Comment on the morphology of the erythrocytes.
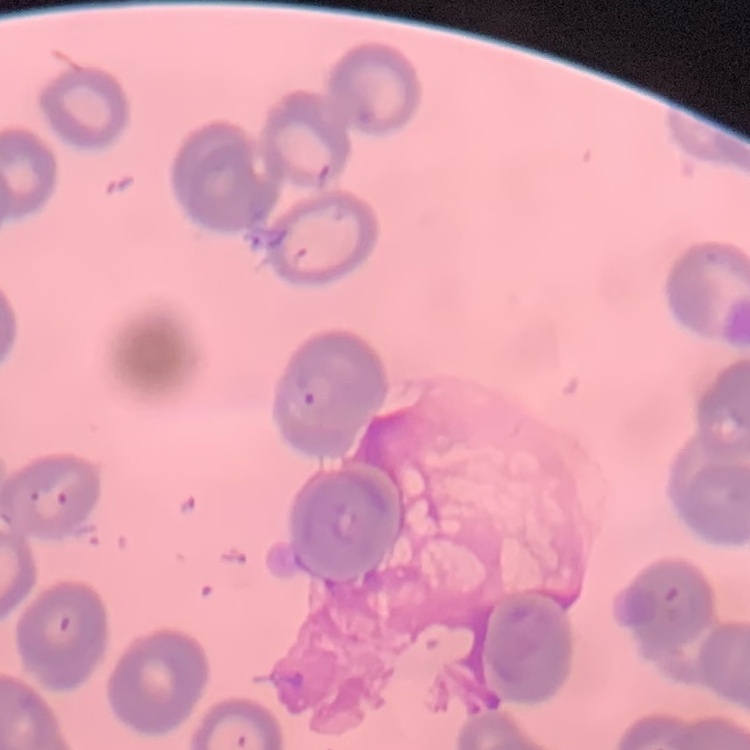
Rouleaux formation.

One tile cut from a larger photomicrograph. Field's or Giemsa stain. Thin blood film.